Classify this cell by malaria status.
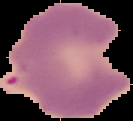
It is parasitized.

preparation = thin blood film
image type = segmented cell region with the area outside set to black
image size = 133×121 pixels